Locate every uninfected red blood cell.
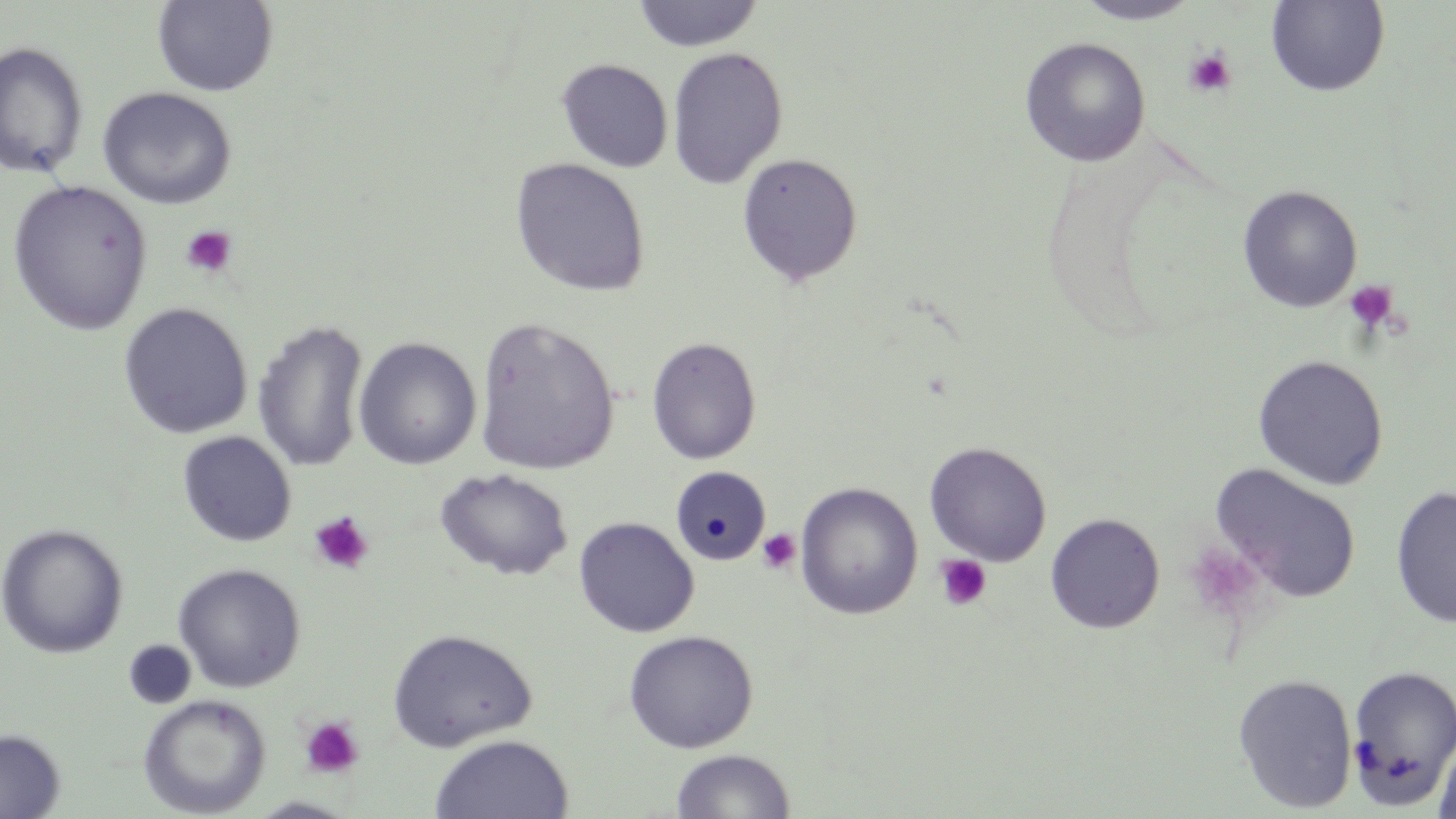
Approximate bounding boxes as [x1, y1, x2, y2] in pixels.
Uninfected red blood cells: [1266, 0, 1390, 96], [151, 1, 279, 96], [632, 1, 764, 52], [1072, 1, 1201, 25], [1019, 37, 1151, 167], [0, 40, 89, 179], [667, 46, 787, 189], [556, 58, 673, 173], [96, 87, 237, 209], [736, 152, 864, 287], [510, 157, 651, 297], [7, 179, 154, 335], [1237, 185, 1363, 313], [118, 302, 253, 439], [473, 316, 620, 476], [253, 319, 370, 473], [646, 335, 762, 465], [354, 337, 482, 470], [1253, 354, 1389, 490], [177, 431, 297, 547], [924, 442, 1052, 566], [1209, 463, 1362, 604], [670, 465, 771, 567], [435, 467, 574, 581], [794, 481, 924, 620], [1390, 485, 1456, 629], [1045, 513, 1165, 634], [573, 516, 699, 637], [0, 523, 129, 659], [172, 562, 306, 692], [386, 627, 537, 751], [622, 629, 759, 753], [123, 640, 197, 709], [1345, 663, 1456, 808], [1232, 673, 1359, 813], [137, 694, 271, 817], [0, 728, 65, 819], [1432, 728, 1456, 819], [430, 734, 574, 819], [670, 748, 796, 818], [247, 796, 358, 818].

slide_level_diagnosis: no evidence of blood parasites
image_size: 1456×819 pixels
preparation: thin blood film
magnification: 1000x
platelet_locations: 'approximate bounding boxes as [x1, y1, x2, y2] in pixels: [1183, 48, 1237, 99], [180, 224, 238, 279], [1343, 279, 1399, 335], [309, 511, 375, 575], [756, 528, 801, 575], [1185, 543, 1268, 622], [934, 554, 992, 611], [299, 715, 365, 779]'
modality: optical microscopy
stain: May-Grünwald-Giemsa
field_of_view: single